Report the malaria status of this cell.
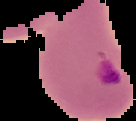
It is parasitized.

image type = segmented cell region on a black background
image size = 136×121 pixels
preparation = thin blood film